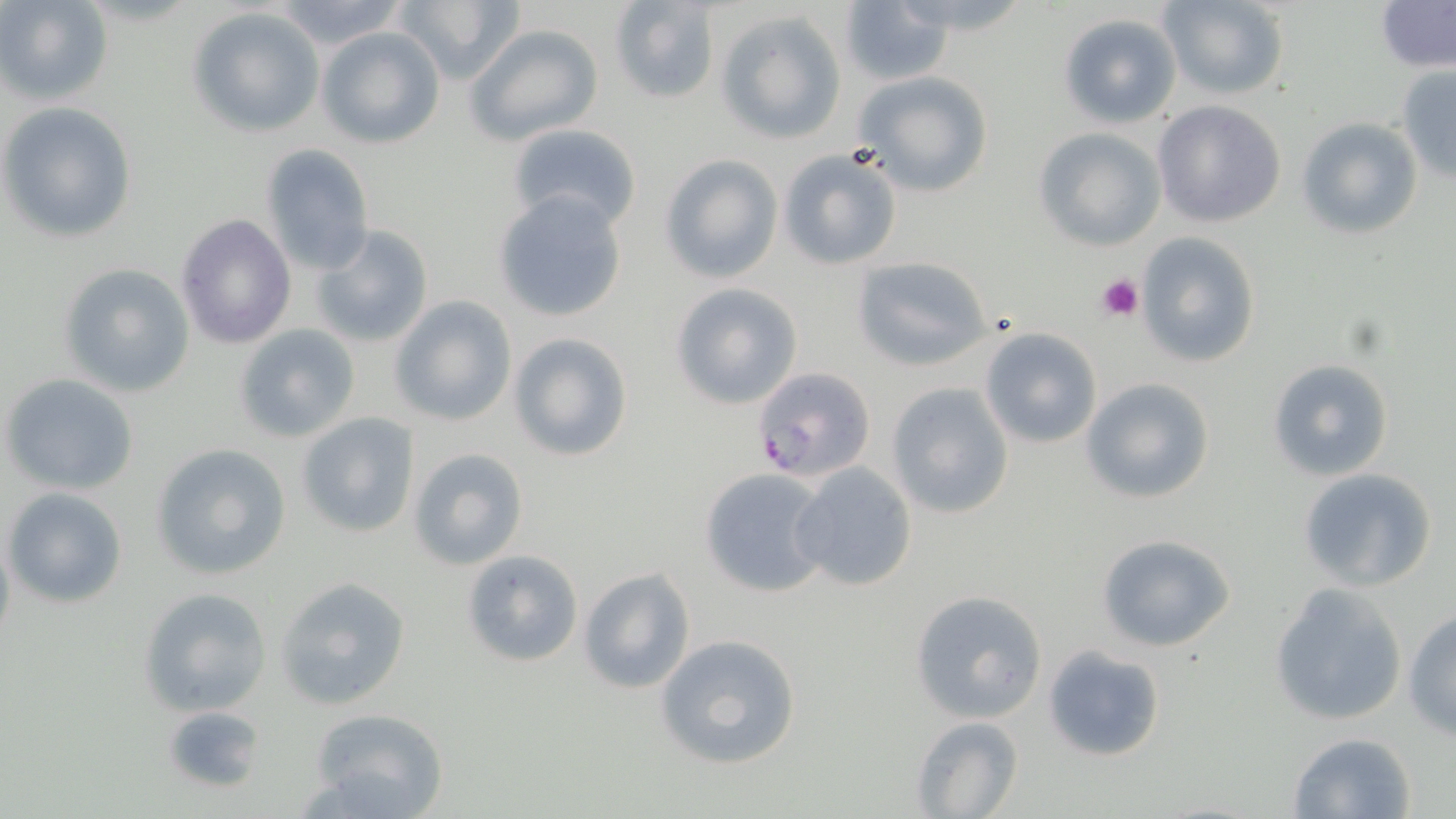

Summary:
  - Coordinate format: approximate bounding boxes as [x1, y1, x2, y2] in pixels
  - Uninfected red blood cell locations: [1, 0, 113, 104], [268, 0, 411, 50], [393, 0, 525, 83], [607, 0, 720, 104], [886, 0, 1037, 37], [1157, 0, 1290, 100], [1377, 0, 1455, 73], [835, 4, 952, 85], [187, 6, 326, 137], [716, 10, 847, 144], [1057, 13, 1181, 128], [466, 24, 603, 146], [317, 26, 445, 149], [1395, 67, 1456, 183], [853, 71, 994, 197], [1153, 100, 1286, 228], [0, 101, 137, 244], [1298, 116, 1423, 238], [506, 123, 642, 234], [1032, 126, 1167, 251], [259, 144, 375, 277], [777, 147, 903, 272], [658, 153, 783, 285], [494, 190, 628, 323], [175, 213, 296, 349], [311, 225, 434, 350], [1134, 233, 1263, 368], [854, 257, 992, 371], [59, 262, 197, 396], [669, 282, 803, 409], [391, 295, 517, 427], [232, 323, 360, 444], [980, 327, 1102, 448], [509, 331, 632, 462], [1267, 358, 1394, 481], [2, 373, 140, 496], [1081, 377, 1216, 504], [886, 383, 1014, 519], [294, 410, 419, 538], [151, 442, 293, 580], [407, 447, 529, 571], [790, 463, 920, 592], [698, 467, 831, 598], [1298, 468, 1438, 592], [4, 485, 127, 608], [0, 526, 15, 651], [1095, 533, 1236, 652], [460, 550, 583, 666], [579, 566, 695, 694], [275, 575, 413, 711], [1267, 582, 1408, 728], [139, 586, 272, 715], [909, 591, 1049, 723], [1403, 609, 1456, 739], [655, 634, 802, 770], [1043, 645, 1167, 762], [162, 704, 264, 794], [308, 707, 449, 818], [910, 715, 1023, 819], [1284, 730, 1418, 819]
  - Plasmodium falciparum-infected red blood cell locations: [751, 365, 875, 485]
  - Platelet locations: [1096, 272, 1144, 321]
  - Slide-level diagnosis: Plasmodium falciparum
  - Image size: 1456×819 pixels
  - Field of view: single
  - Modality: light microscopy
  - Preparation: thin blood film
  - Magnification: 1000x
  - Stain: May-Grünwald-Giemsa